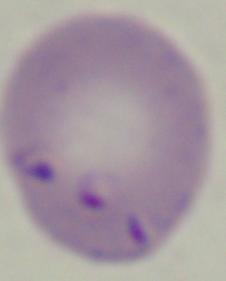
modality = photomicrograph
magnification = 1000x
identification = Babesia